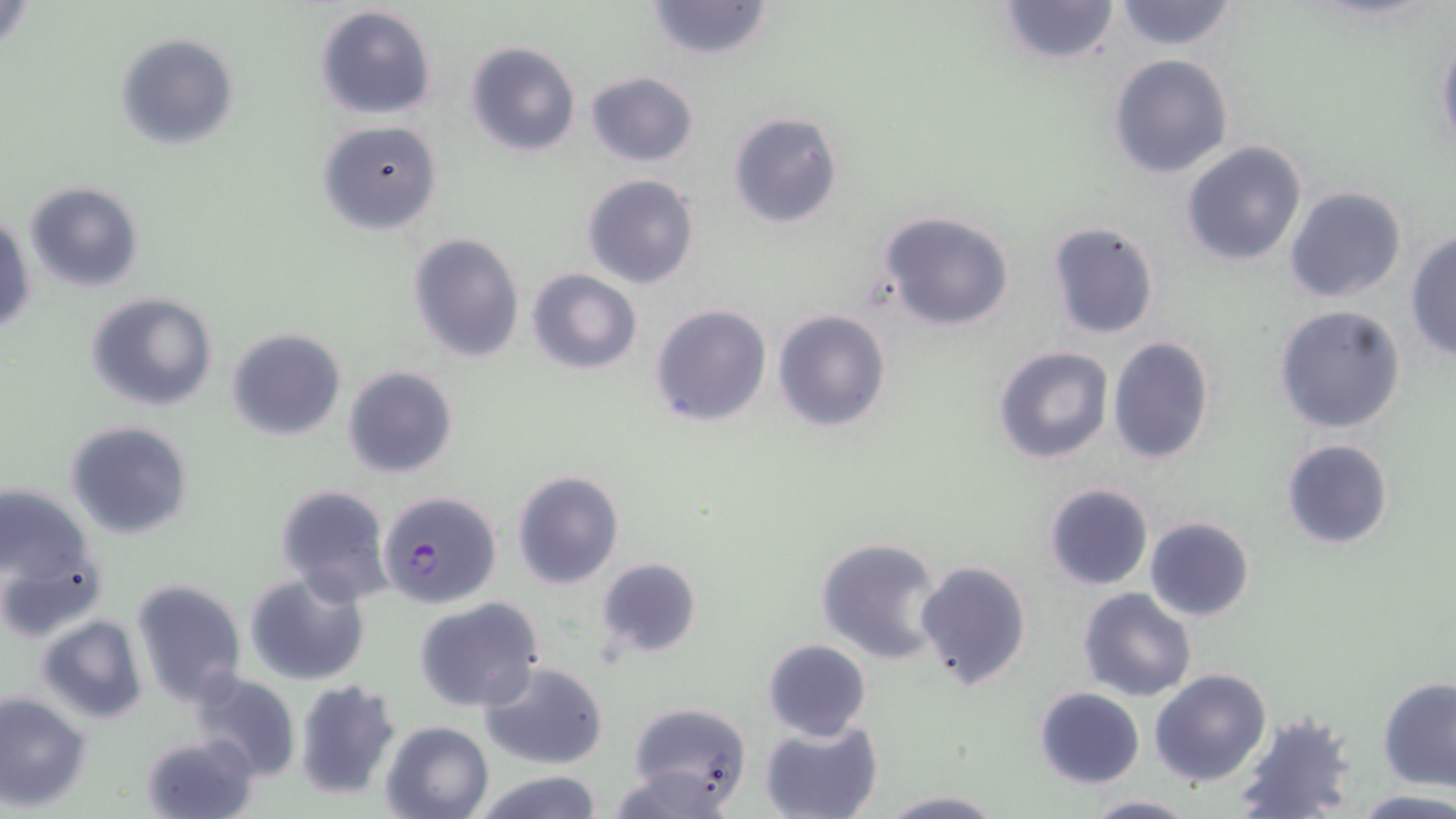

slide-level diagnosis = Plasmodium falciparum
preparation = thin blood smear
modality = light microscopy
stain = May-Grünwald-Giemsa
uninfected red blood cell locations = approximate bounding boxes as (x1, y1, x2, y2) in pixels: (642, 0, 776, 61), (997, 0, 1121, 66), (1110, 0, 1240, 52), (314, 5, 437, 119), (1435, 31, 1456, 163), (114, 33, 239, 150), (465, 41, 580, 156), (1108, 53, 1235, 178), (583, 70, 699, 167), (728, 110, 844, 230), (317, 119, 442, 235), (1180, 140, 1308, 266), (581, 174, 700, 289), (23, 180, 144, 295), (1284, 185, 1408, 304), (878, 209, 1018, 332), (1, 210, 35, 336), (1046, 221, 1159, 339), (1405, 229, 1456, 362), (407, 231, 525, 363), (526, 269, 642, 375), (86, 292, 218, 411), (649, 303, 773, 427), (1272, 303, 1406, 435), (772, 309, 891, 432), (226, 327, 346, 440), (1106, 334, 1216, 467), (991, 345, 1114, 465), (342, 365, 458, 480), (64, 421, 193, 540), (1280, 438, 1394, 550), (511, 469, 626, 590), (0, 481, 97, 617), (1043, 483, 1153, 591), (274, 484, 393, 604), (1145, 516, 1254, 622), (814, 535, 947, 665), (595, 557, 702, 659), (915, 559, 1032, 691), (243, 570, 369, 685), (130, 577, 247, 706), (1079, 586, 1195, 701), (412, 596, 544, 712), (36, 614, 147, 724), (761, 638, 871, 741), (478, 660, 610, 769), (1150, 668, 1271, 786), (187, 670, 301, 783), (1378, 676, 1456, 793), (292, 678, 402, 801), (1033, 686, 1145, 788), (0, 692, 91, 810), (621, 702, 753, 813), (1233, 713, 1359, 819), (758, 718, 883, 819), (379, 719, 493, 819), (142, 733, 258, 818), (471, 770, 605, 819), (1347, 789, 1456, 818), (877, 791, 1007, 819), (1082, 793, 1199, 818)
magnification = 1000x
Plasmodium falciparum-infected red blood cell locations = approximate bounding boxes as (x1, y1, x2, y2) in pixels: (377, 489, 502, 609)
field of view = single
image size = 1456×819 pixels